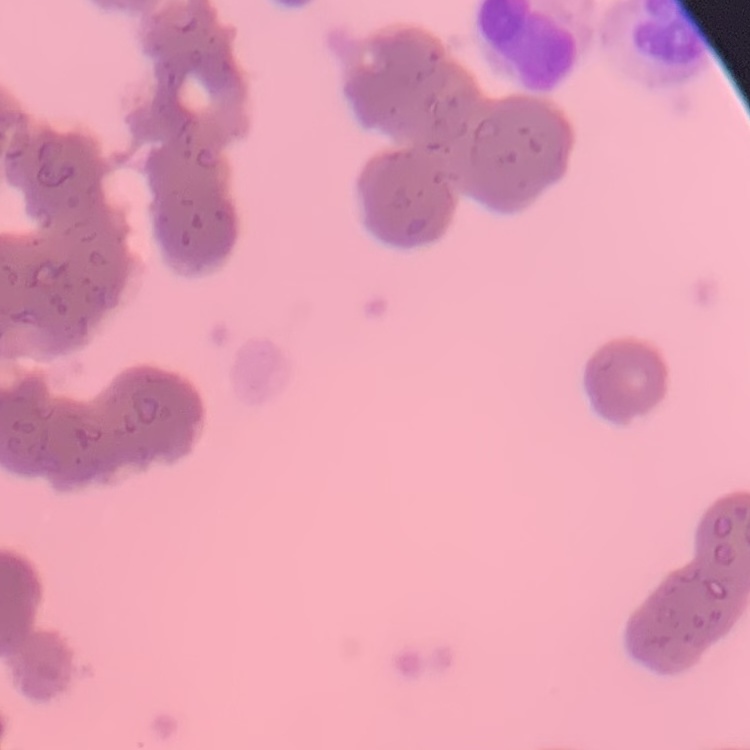
red_blood_cell_morphology: rouleaux formation
stain: Field's or Giemsa
image_type: square crop of a larger photomicrograph
preparation: thin blood smear